Classify this cell by malaria status.
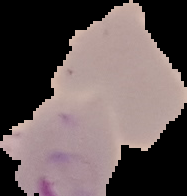
Uninfected.

Summary:
  - Image type: segmented cell region on a black background
  - Preparation: thin blood film
  - Image size: 187×196 pixels